Report the malaria status of this cell.
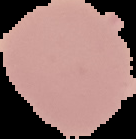
It is uninfected.

Image is 136×139 pixels. Cell region segmented out of the field of view; the surrounding area is masked to black. From a thin blood film.